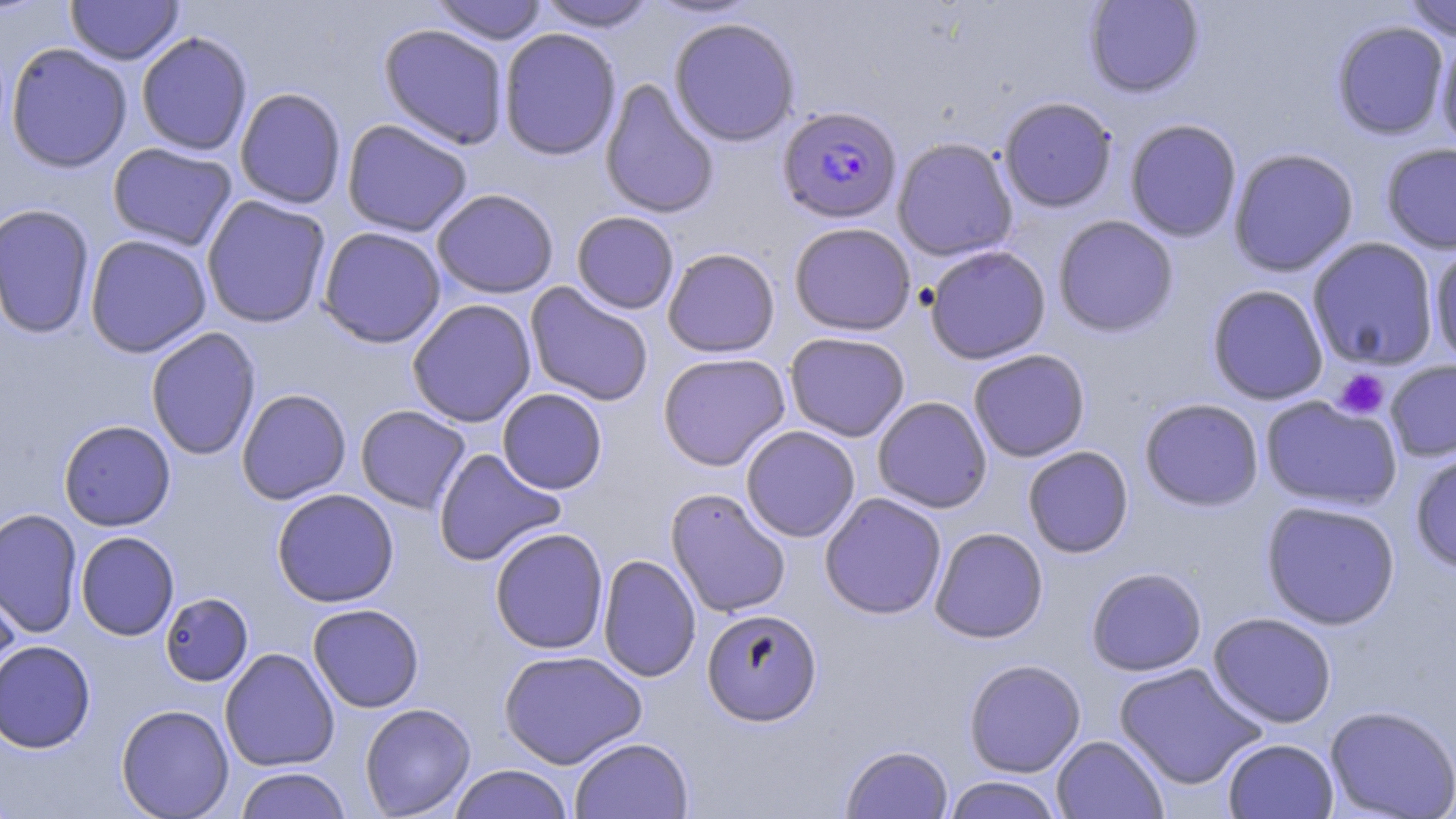 Approximate bounding boxes as named x1/y1/x2/y2 corners in pixels. Platelet locations: (x1=1335, y1=369, x2=1390, y2=419). Uninfected red blood cell locations: (x1=66, y1=0, x2=183, y2=65), (x1=431, y1=0, x2=549, y2=45), (x1=644, y1=0, x2=761, y2=20), (x1=1083, y1=0, x2=1204, y2=97), (x1=1402, y1=0, x2=1456, y2=41), (x1=534, y1=1, x2=660, y2=32), (x1=668, y1=17, x2=801, y2=147), (x1=1331, y1=20, x2=1450, y2=140), (x1=378, y1=23, x2=510, y2=150), (x1=498, y1=27, x2=622, y2=161), (x1=136, y1=31, x2=253, y2=156), (x1=1434, y1=31, x2=1456, y2=157), (x1=5, y1=42, x2=133, y2=172), (x1=600, y1=79, x2=720, y2=219), (x1=234, y1=87, x2=347, y2=209), (x1=999, y1=96, x2=1118, y2=213), (x1=1124, y1=118, x2=1242, y2=242), (x1=341, y1=119, x2=473, y2=237), (x1=891, y1=137, x2=1018, y2=261), (x1=107, y1=142, x2=238, y2=251), (x1=1381, y1=143, x2=1456, y2=254), (x1=1228, y1=147, x2=1359, y2=277), (x1=431, y1=188, x2=559, y2=298), (x1=201, y1=195, x2=331, y2=329), (x1=0, y1=203, x2=96, y2=339), (x1=571, y1=211, x2=679, y2=314), (x1=1052, y1=214, x2=1179, y2=337), (x1=788, y1=222, x2=916, y2=335), (x1=317, y1=226, x2=446, y2=348), (x1=84, y1=234, x2=212, y2=358), (x1=1307, y1=237, x2=1440, y2=371), (x1=1428, y1=243, x2=1456, y2=368), (x1=924, y1=245, x2=1051, y2=364), (x1=662, y1=247, x2=780, y2=358), (x1=524, y1=282, x2=654, y2=407), (x1=1207, y1=284, x2=1329, y2=405), (x1=407, y1=299, x2=537, y2=427), (x1=145, y1=327, x2=262, y2=461), (x1=784, y1=331, x2=910, y2=442), (x1=967, y1=349, x2=1090, y2=462), (x1=657, y1=352, x2=791, y2=471), (x1=1383, y1=360, x2=1456, y2=462), (x1=236, y1=388, x2=352, y2=505), (x1=496, y1=388, x2=607, y2=494), (x1=871, y1=396, x2=993, y2=513), (x1=1260, y1=396, x2=1403, y2=511), (x1=1139, y1=397, x2=1264, y2=511), (x1=355, y1=405, x2=471, y2=514), (x1=58, y1=420, x2=176, y2=531), (x1=740, y1=425, x2=861, y2=543), (x1=1022, y1=445, x2=1134, y2=558), (x1=433, y1=448, x2=566, y2=567), (x1=1410, y1=451, x2=1456, y2=574), (x1=665, y1=487, x2=792, y2=618), (x1=271, y1=488, x2=399, y2=607), (x1=819, y1=492, x2=947, y2=619), (x1=1260, y1=499, x2=1401, y2=630), (x1=0, y1=508, x2=83, y2=638), (x1=489, y1=527, x2=609, y2=654), (x1=929, y1=527, x2=1048, y2=643), (x1=75, y1=531, x2=179, y2=640), (x1=597, y1=554, x2=701, y2=682), (x1=1085, y1=566, x2=1207, y2=676), (x1=0, y1=575, x2=22, y2=698), (x1=160, y1=592, x2=254, y2=686), (x1=307, y1=603, x2=424, y2=713), (x1=701, y1=608, x2=822, y2=726), (x1=1207, y1=612, x2=1337, y2=728), (x1=0, y1=640, x2=96, y2=754), (x1=219, y1=648, x2=340, y2=772), (x1=498, y1=649, x2=647, y2=768), (x1=963, y1=658, x2=1086, y2=777), (x1=1113, y1=662, x2=1267, y2=790), (x1=359, y1=703, x2=476, y2=817), (x1=115, y1=704, x2=234, y2=818), (x1=1324, y1=704, x2=1455, y2=818), (x1=1051, y1=735, x2=1168, y2=819), (x1=569, y1=737, x2=693, y2=818), (x1=1222, y1=738, x2=1339, y2=818), (x1=841, y1=744, x2=953, y2=818), (x1=449, y1=764, x2=573, y2=819), (x1=233, y1=767, x2=351, y2=818), (x1=942, y1=775, x2=1064, y2=819). Plasmodium falciparum-infected red blood cell locations: (x1=778, y1=107, x2=902, y2=225). Slide-level diagnosis: Plasmodium falciparum. Single field of view. Light microscopy. May-Grünwald-Giemsa-stained preparation. Captured at 1000x magnification. Thin blood film. Image is 1456×819 pixels.